Look for Plasmodium parasites.
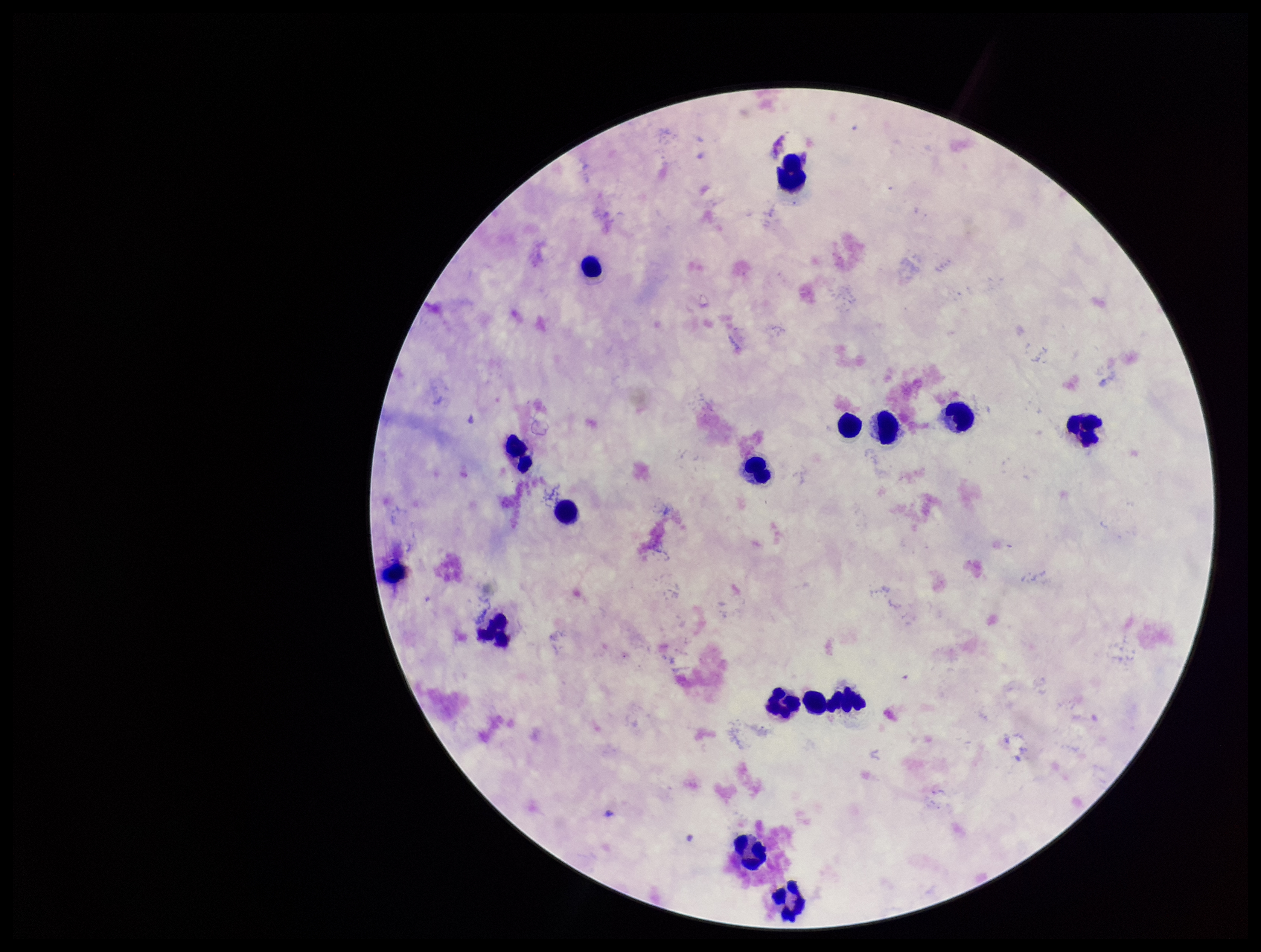

None identified.

Summary:
  - Patient malaria status: negative
  - Stain: Giemsa
  - Parasite count: 0
  - Leukocyte count: 15
  - Image size: 1261×952 pixels
  - Capture: smartphone photograph through the microscope eyepiece
  - Field of view: one from this slide
  - Preparation: thick smear